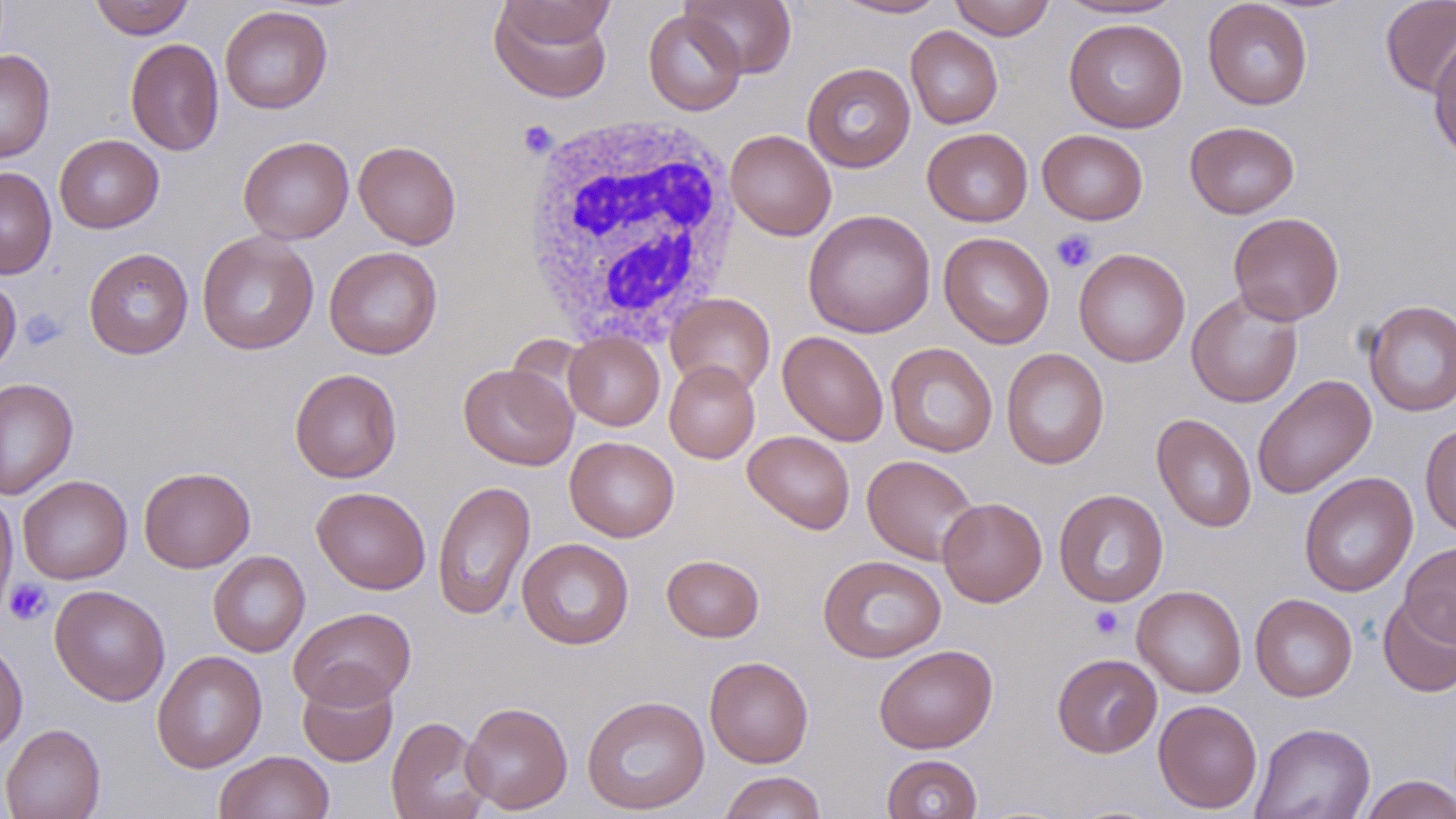

Summary:
  - Coordinate format: approximate bounding boxes as (x1,y1)-(x2,y2) corner pairs in pixels
  - White blood cell locations: (519,113)-(743,346)
  - Platelet locations: (518,121)-(558,159), (1050,229)-(1097,273), (19,309)-(68,348), (3,579)-(53,625), (1089,605)-(1124,639)
  - Uninfected red blood cell locations: (89,0)-(194,39), (496,0)-(617,50), (682,0)-(797,78), (832,0)-(950,19), (949,0)-(1055,40), (1057,0)-(1185,20), (1380,0)-(1456,98), (1202,1)-(1313,110), (489,3)-(614,103), (220,6)-(333,114), (643,9)-(747,116), (1064,18)-(1187,133), (905,26)-(1003,129), (1429,37)-(1456,164), (125,38)-(224,157), (0,49)-(55,164), (802,62)-(916,172), (1185,121)-(1300,219), (922,128)-(1032,227), (725,129)-(836,240), (1037,129)-(1148,225), (54,134)-(164,233), (238,136)-(354,244), (353,140)-(461,249), (0,167)-(57,279), (803,209)-(936,338), (1228,212)-(1344,325), (196,231)-(319,355), (938,232)-(1054,348), (324,246)-(442,359), (83,247)-(194,359), (1074,248)-(1190,367), (0,276)-(21,377), (1187,291)-(1303,408), (665,293)-(775,397), (1362,299)-(1456,417), (564,331)-(665,431), (777,331)-(889,446), (885,342)-(998,458), (1001,348)-(1110,470), (664,361)-(760,463), (458,363)-(578,470), (289,368)-(402,483), (1252,375)-(1377,499), (0,377)-(79,499), (1152,413)-(1256,533), (1420,424)-(1456,537), (743,430)-(855,534), (564,436)-(679,542), (862,454)-(980,565), (138,467)-(255,572), (1299,472)-(1418,597), (17,475)-(132,584), (432,480)-(536,621), (311,486)-(430,594), (1053,488)-(1169,607), (0,489)-(17,624), (937,497)-(1047,607), (517,538)-(634,649), (1399,541)-(1456,646), (208,550)-(310,657), (662,554)-(764,642), (817,555)-(947,663), (50,585)-(170,705), (1133,585)-(1247,698), (1250,593)-(1357,702), (1378,594)-(1456,697), (288,607)-(417,710), (0,639)-(28,754), (874,644)-(998,754), (152,650)-(267,772), (1052,653)-(1162,757), (705,656)-(813,767), (297,671)-(398,767), (582,694)-(710,815), (1153,699)-(1262,813), (461,701)-(573,814), (386,717)-(491,819), (1251,722)-(1376,819), (0,724)-(105,819), (214,750)-(335,819), (881,754)-(983,818), (719,770)-(827,819), (1358,774)-(1456,819)
  - Slide-level diagnosis: negative for blood parasites
  - Preparation: thin blood film
  - Magnification: 1000x
  - Field of view: single
  - Modality: optical microscopy
  - Stain: May-Grünwald-Giemsa
  - Image size: 1456×819 pixels